Report the malaria status of this cell.
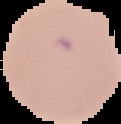

It is parasitized.

Segmented cell region on a black background. From a thin blood smear. Image is 121×124 pixels.